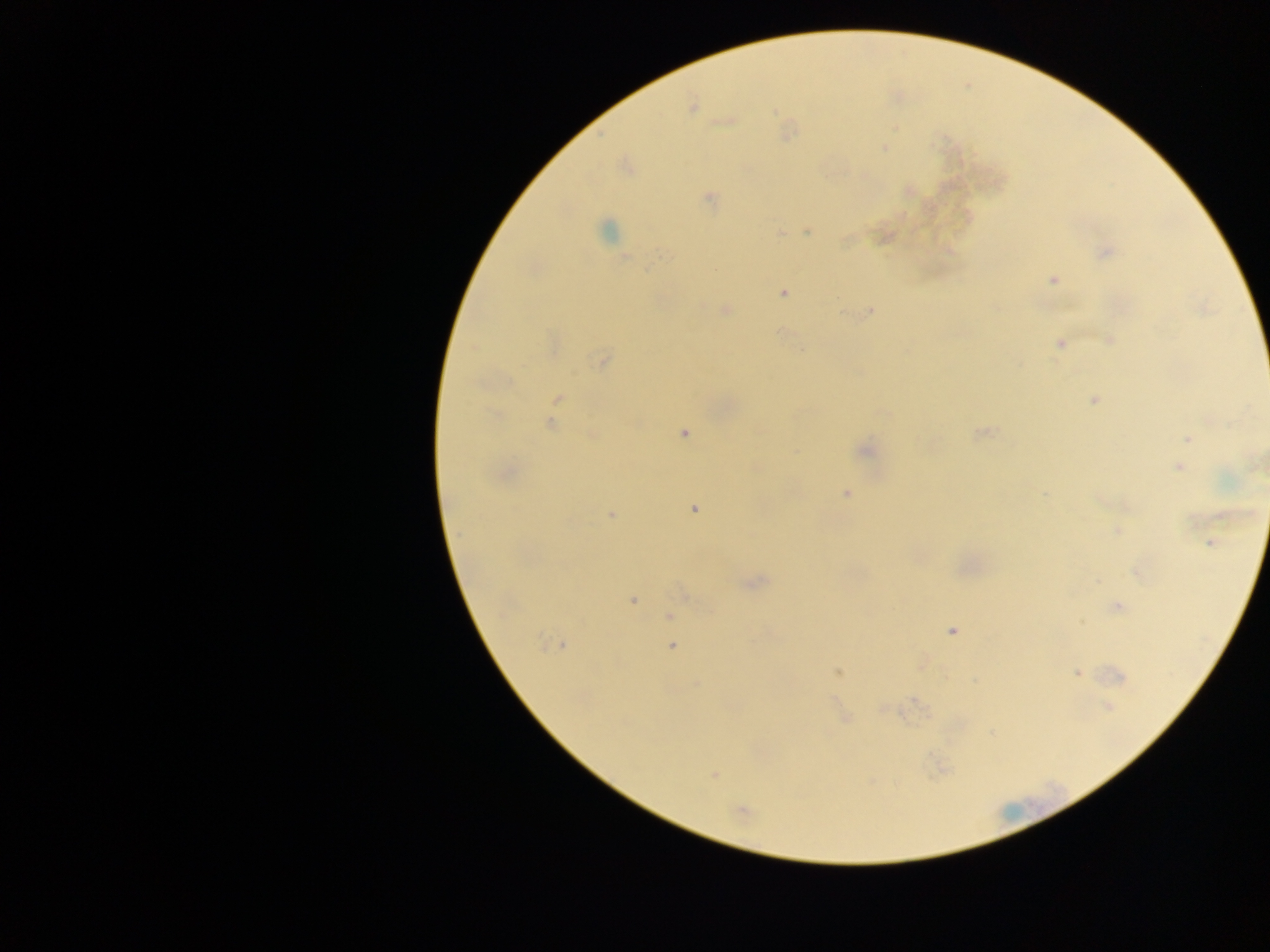 Approximate centers as [x, y] in pixels. Plasmodium parasite locations: [692, 107], [727, 121], [884, 148], [708, 198], [606, 231], [807, 231], [780, 233], [845, 241], [1105, 253], [647, 269], [1053, 279], [783, 293], [725, 310], [871, 310], [842, 312], [1109, 340], [1059, 343], [602, 361], [558, 398], [1094, 400], [883, 413], [1212, 419], [551, 425], [684, 433], [980, 433], [1188, 438], [865, 451], [1182, 455], [1179, 467], [1043, 493], [845, 494], [694, 509], [611, 515], [1118, 531], [1210, 543], [1137, 573], [754, 582], [685, 594], [632, 600], [1118, 606], [669, 616], [951, 631], [558, 645], [672, 646], [838, 672], [1077, 673], [1120, 676], [696, 683], [916, 700], [1108, 707], [713, 775], [741, 810]. One field of view. Sample from Ghana. Image is 1270×952 pixels. Thick blood film. Photographed through a microscope with a mobile-phone camera.